Point out each Plasmodium parasite.
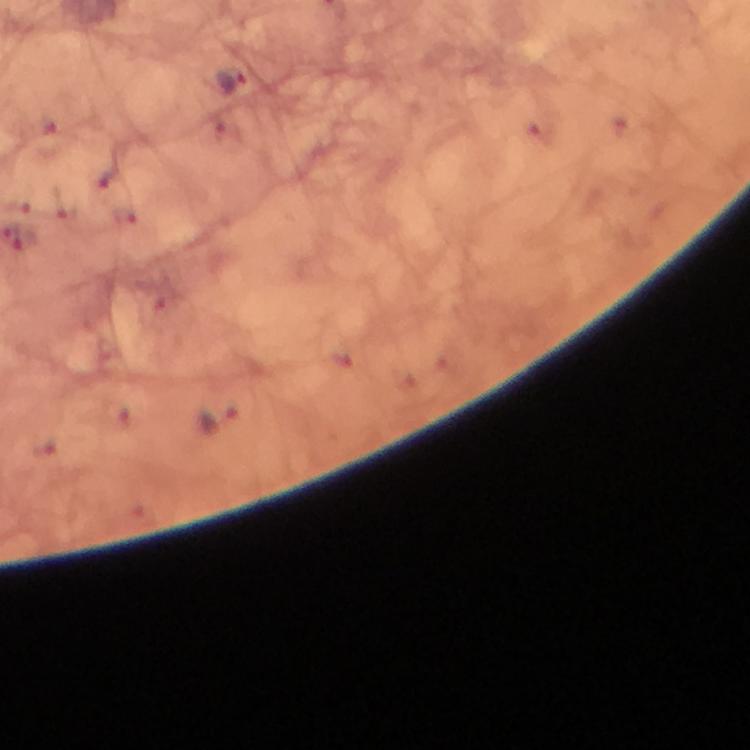

Approximate centers as (x, y) in pixels.
Plasmodium parasites: (230, 80), (220, 419).

{
  "magnification": "100x",
  "immersion_oil": "used",
  "cropped_from": "one field of view",
  "stain": "Giemsa",
  "image_size": "750×750 pixels",
  "context": "from a diagnostic examination for malaria",
  "capture": "smartphone photograph through a microscope",
  "preparation": "thick smear"
}